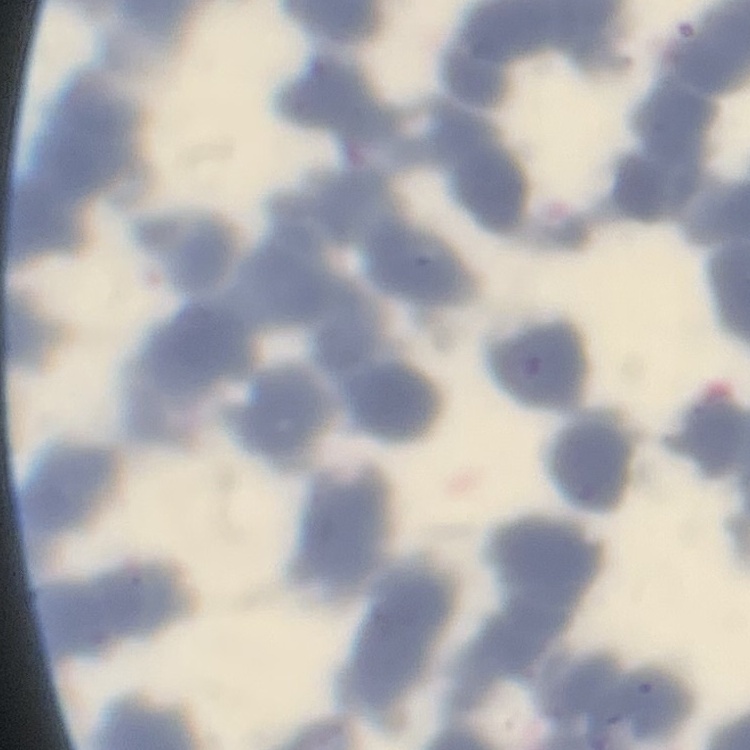
Summary:
  - Red blood cell morphology: rouleaux formation
  - Preparation: thin blood film
  - Stain: Field's or Giemsa
  - Image type: one tile cut from a larger photomicrograph